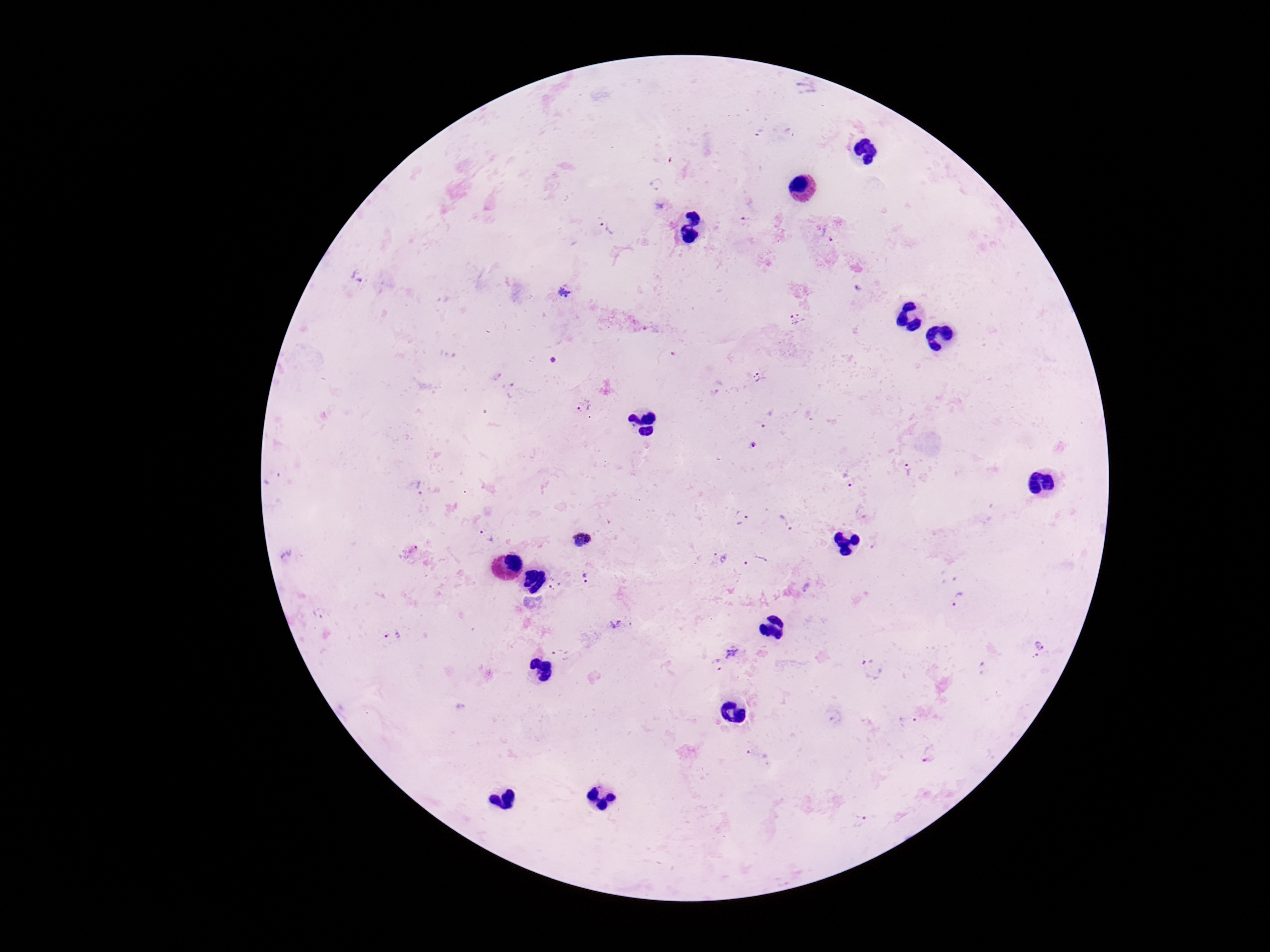
patient_malaria_status: infected
image_size: 1270×952 pixels
preparation: thick peripheral-blood smear
field_of_view: single
stain: Giemsa
capture: smartphone camera through the microscope eyepiece
plasmodium_parasite_locations: 'approximate centers as (x, y) in pixels: (655, 184), (604, 225), (358, 274), (565, 293), (797, 320), (758, 379), (584, 405), (769, 418), (755, 446), (909, 470), (849, 482), (741, 520), (785, 523), (487, 536), (581, 541), (718, 559), (756, 563), (585, 580), (554, 584), (959, 599), (615, 623), (393, 637), (1041, 644), (733, 653), (561, 656), (716, 664), (873, 669), (907, 722), (758, 755), (929, 755), (861, 821)'
magnification: 100x